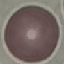

Summary:
  - Result: negative for malaria parasites
  - Preparation: thin blood smear
  - Capture: smartphone camera at the microscope eyepiece
  - Image type: automatically extracted cell patch, resized to 64 × 64 pixels
  - Stain: Giemsa